Name the cell type shown.
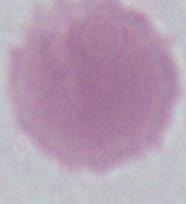

An erythrocyte.

Summary:
  - Magnification: 1000x
  - Modality: micrograph